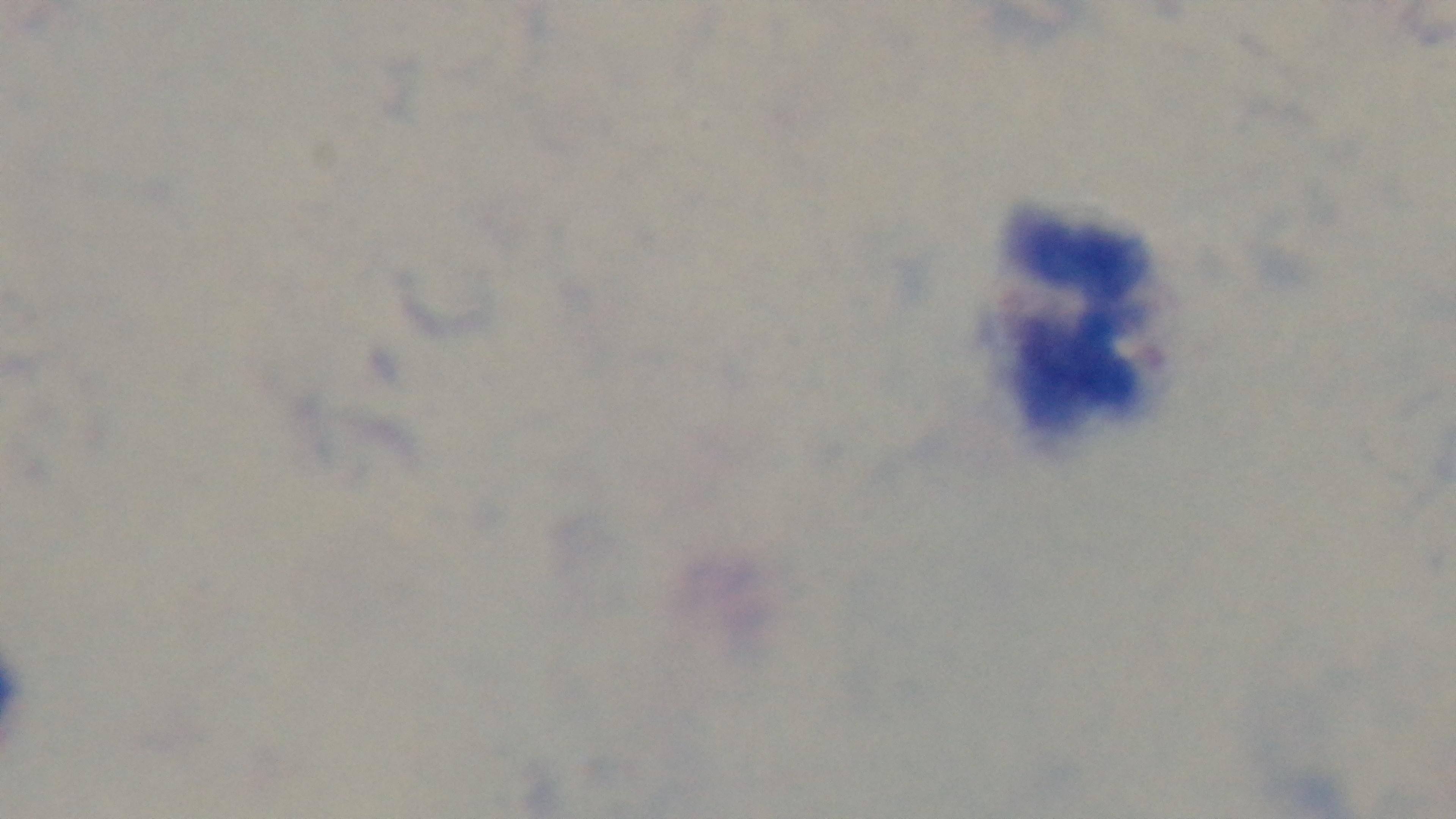

Malaria status: negative. Preparation: thick blood film. Captured with a mounted 4K digital camera. Giemsa stain. Single field of view. 100x oil-immersion objective. Light microscopy.